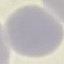

result = no malaria parasites detected
preparation = thin smear
image type = cell patch, automatically extracted from a larger field of view and resized to 64 × 64 pixels
stain = Giemsa
capture = smartphone through the microscope eyepiece